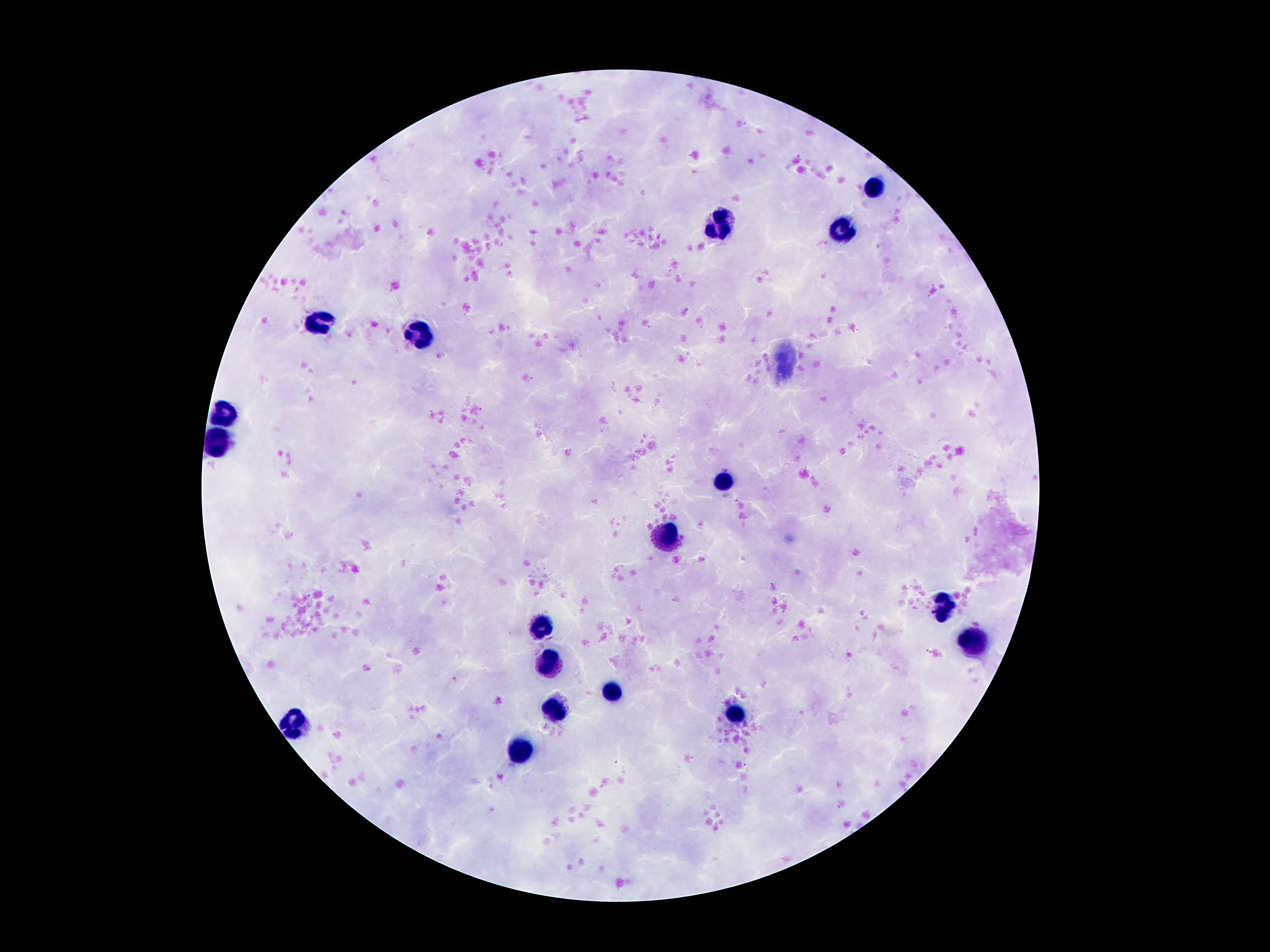

patient_malaria_status: negative
magnification: 100x
image_size: 1270×952 pixels
capture: smartphone camera through the microscope eyepiece
preparation: thick peripheral-blood smear
leukocyte_locations: 'approximate centers as (x, y) in pixels: (874, 184), (720, 219), (839, 229), (322, 322), (421, 332), (222, 411), (218, 442), (724, 481), (669, 536), (943, 602), (542, 623), (974, 638), (551, 662), (609, 693), (554, 709), (735, 716), (293, 724), (520, 747)'
field_of_view: single
stain: Giemsa